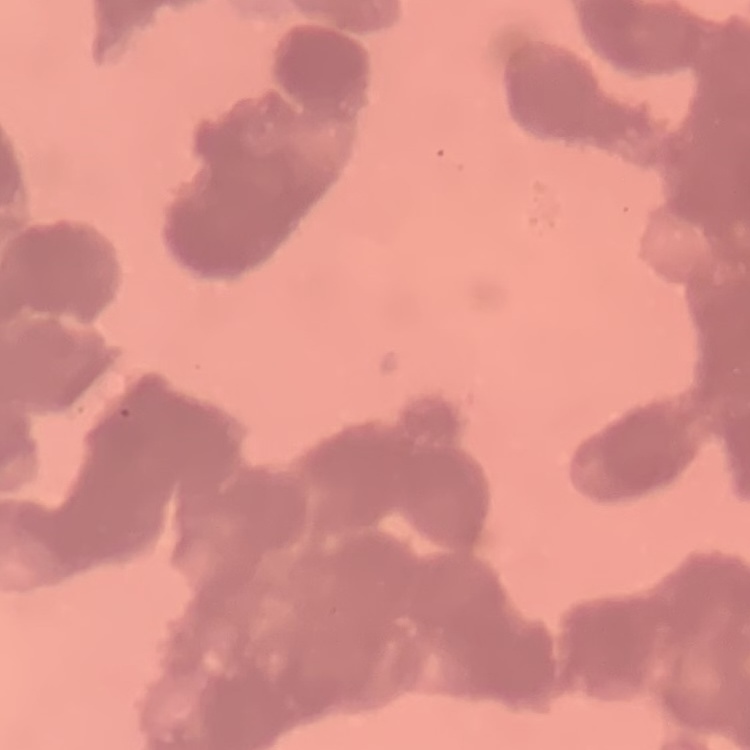

{
  "erythrocyte_morphology": "rouleaux formation",
  "stain": "Field's or Giemsa",
  "image_type": "one tile cut from a larger photomicrograph",
  "preparation": "thin blood smear"
}